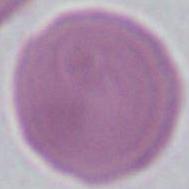
Summary:
  - Identification: erythrocyte
  - Magnification: 1000x
  - Modality: micrograph